State which parasite is depicted.
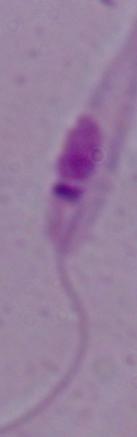

This is Leishmania.

magnification = 1000x
modality = photomicrograph